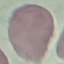
Result: no malaria parasites seen. Giemsa stain. Photographed with a smartphone camera at the microscope eyepiece. Thin blood smear. Cell patch, automatically extracted from a larger field of view and resized to 64 × 64 pixels.